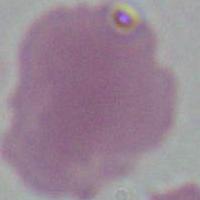

An erythrocyte is seen. Photomicrograph. 1000x magnification.